Name the parasite shown.
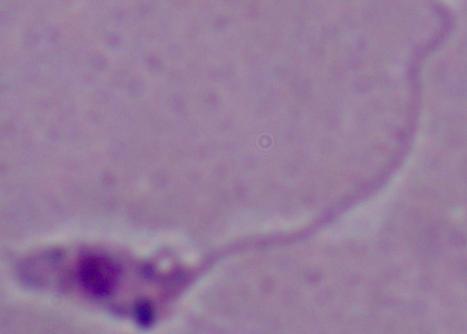

This is Leishmania.

modality = micrograph
magnification = 1000x